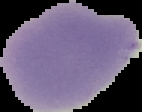
From a thin blood smear. Malaria status: uninfected. Segmented cell region on a black background. Image is 142×112 pixels.